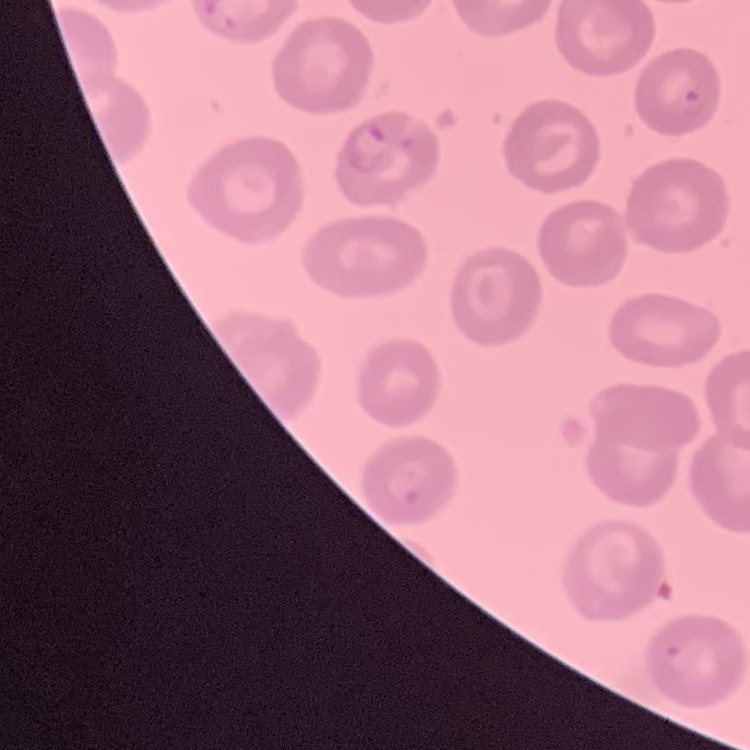

Summary:
  - Erythrocyte morphology: no rouleaux formation
  - Stain: Field's or Giemsa
  - Preparation: thin peripheral smear
  - Image type: square crop of a larger photomicrograph